Evaluate for parasitized red blood cells.
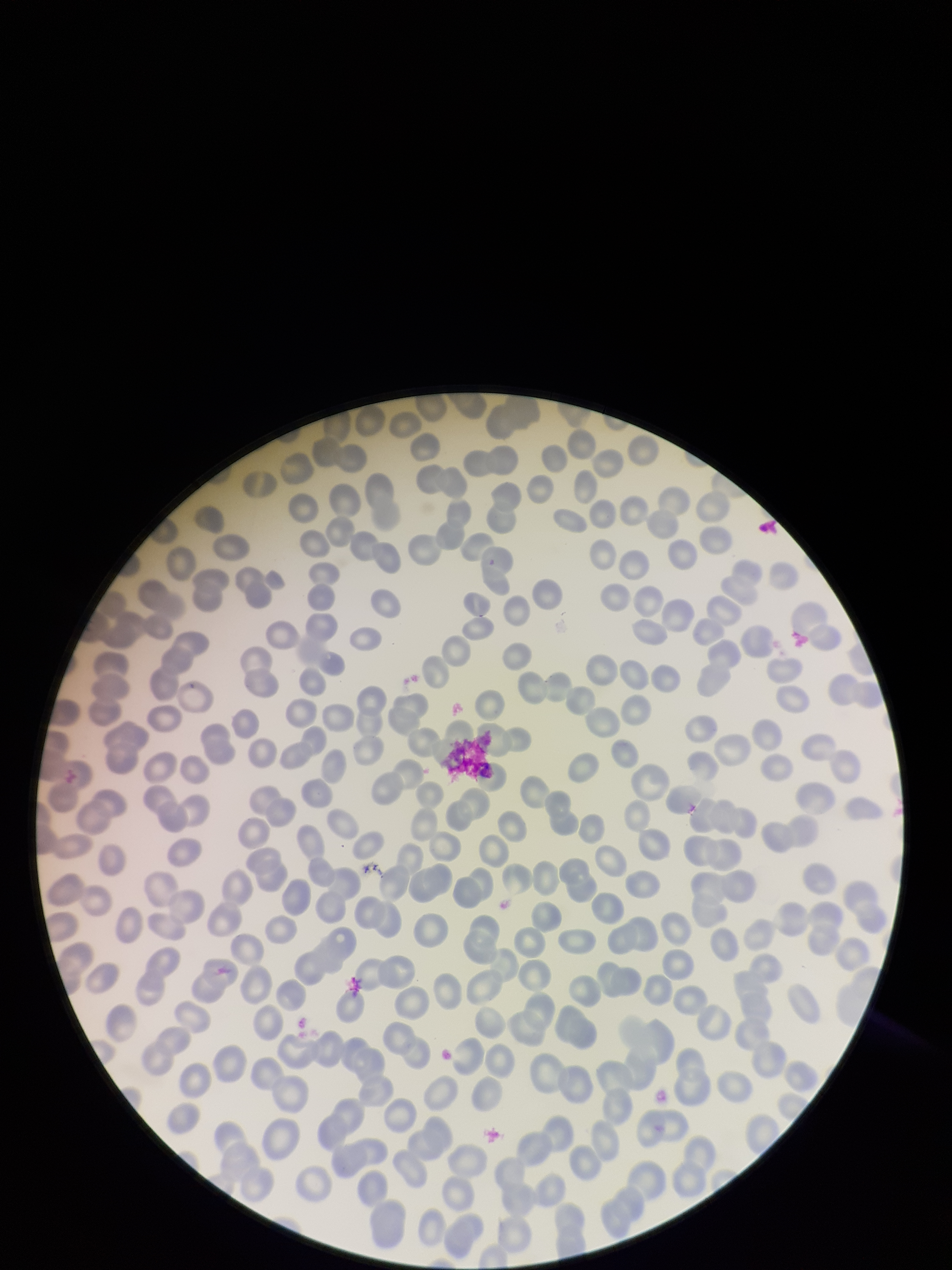
None seen.

Summary:
  - Red blood cell count: 262
  - Stain: Giemsa
  - Preparation: thin blood smear
  - Field of view: single
  - Capture: smartphone photograph through the microscope eyepiece
  - Image size: 952×1270 pixels
  - Patient malaria status: negative
  - Parasitized red blood cell count: 0